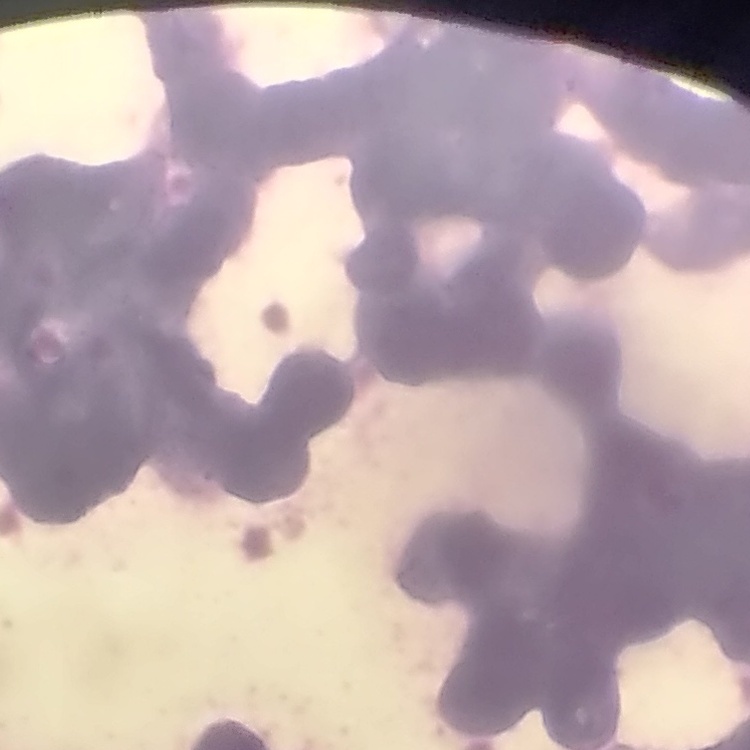

Summary:
  - Erythrocyte morphology: rouleaux formation
  - Image type: one tile cut from a larger photomicrograph
  - Stain: Field's or Giemsa
  - Preparation: thin peripheral smear